Report the malaria status of this cell.
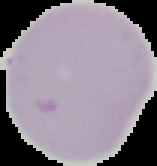

Uninfected.

image size = 157×166 pixels
image type = segmented cell region with the area outside set to black
preparation = thin blood film